Describe the morphology of the erythrocytes.
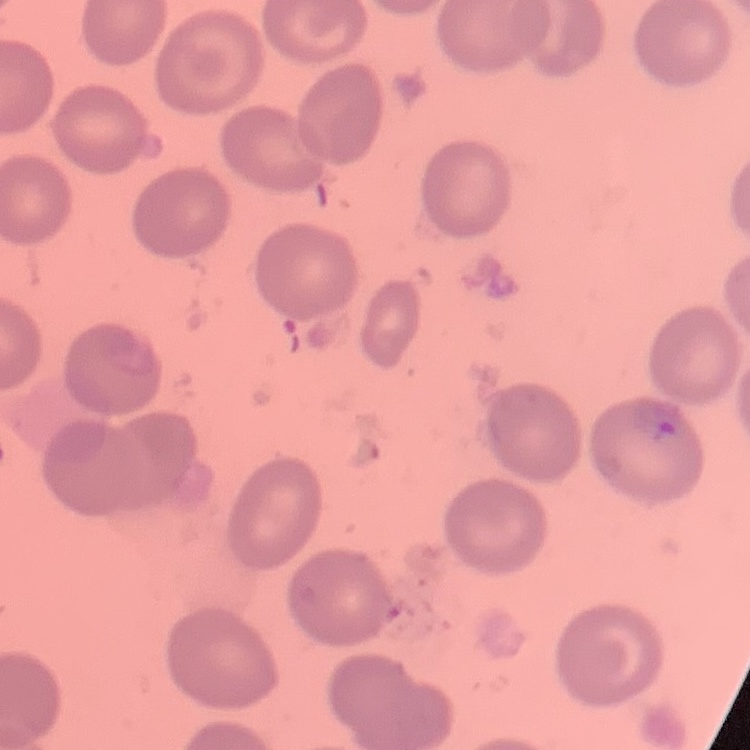
No rouleaux formation.

image type = square crop of a larger photomicrograph
preparation = thin blood film
stain = Field's or Giemsa